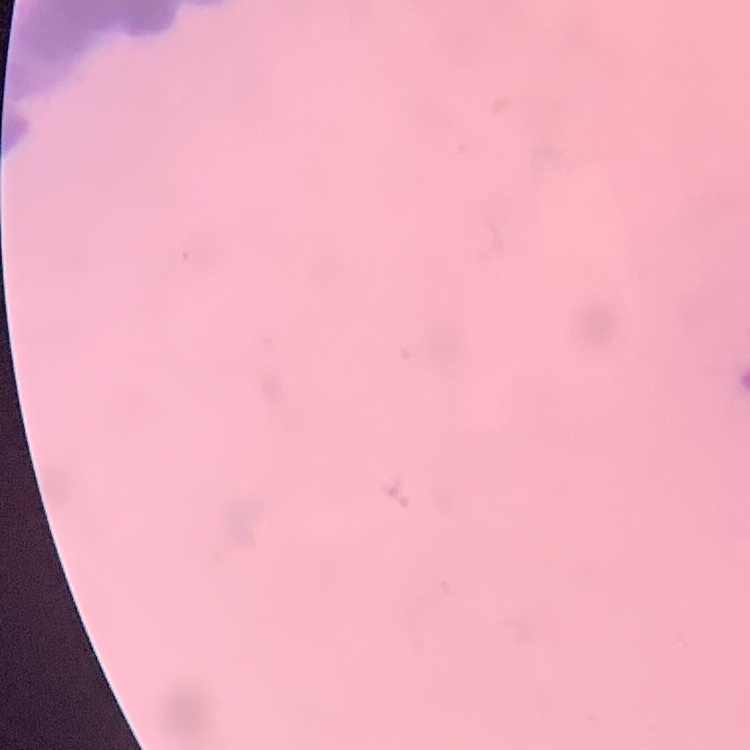
Summary:
  - Erythrocyte morphology: rouleaux formation
  - Stain: Field's or Giemsa
  - Image type: one tile cut from a larger photomicrograph
  - Preparation: thin peripheral smear